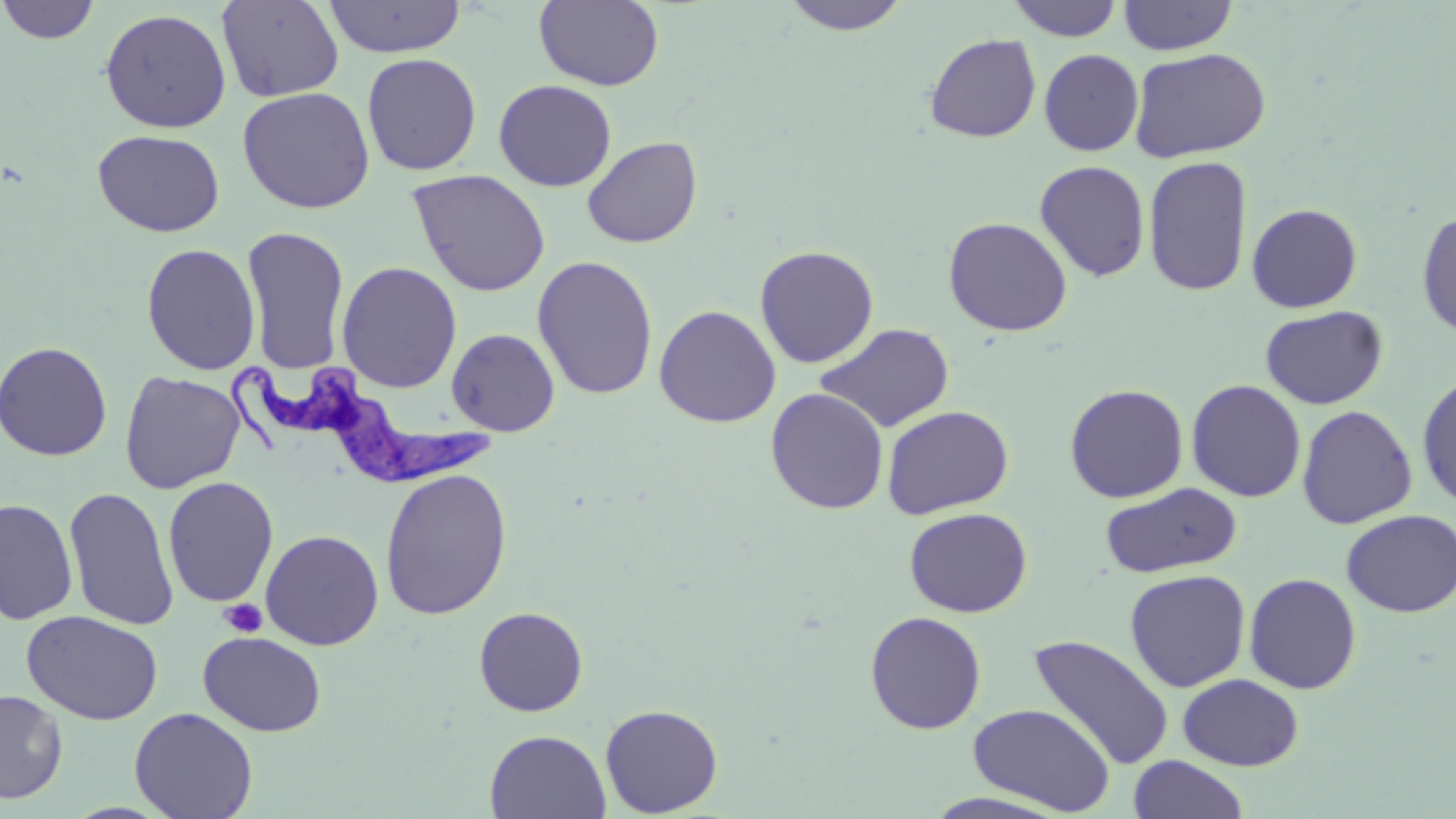
Summary:
  - Coordinate format: approximate bounding boxes as (x1,y1)-(x2,y2) corner pairs in pixels
  - Platelet locations: (219,598)-(267,638)
  - Trypanosoma brucei locations: (233,359)-(498,487)
  - Uninfected red blood cell locations: (0,0)-(101,45), (216,0)-(344,103), (534,0)-(665,91), (778,0)-(914,36), (1007,0)-(1124,41), (1118,0)-(1238,55), (323,1)-(467,58), (99,8)-(232,133), (924,33)-(1042,142), (1128,48)-(1272,163), (1039,49)-(1143,156), (362,53)-(482,176), (493,79)-(616,191), (237,86)-(375,213), (92,129)-(226,237), (582,136)-(703,249), (1143,155)-(1253,297), (1034,160)-(1151,282), (408,169)-(551,297), (1247,203)-(1363,313), (1416,210)-(1456,341), (943,216)-(1072,337), (241,226)-(350,373), (141,243)-(261,375), (754,244)-(878,368), (532,255)-(659,400), (337,261)-(462,393), (654,305)-(781,427), (1260,306)-(1389,410), (815,323)-(955,433), (446,328)-(560,437), (0,340)-(113,461), (120,370)-(245,493), (1416,372)-(1456,511), (1186,379)-(1306,502), (1064,384)-(1189,503), (765,388)-(889,514), (881,405)-(1014,519), (1297,405)-(1418,529), (379,468)-(513,620), (162,476)-(279,607), (1099,482)-(1243,579), (62,487)-(179,631), (0,497)-(78,625), (903,506)-(1032,617), (1341,509)-(1456,618), (261,530)-(384,650), (1124,569)-(1251,692), (1244,572)-(1362,694), (473,606)-(589,717), (22,610)-(163,725), (864,611)-(987,735), (198,631)-(326,736), (1028,633)-(1175,772), (1177,673)-(1304,771), (0,688)-(68,804), (600,703)-(723,817), (967,703)-(1116,815), (129,706)-(259,819), (485,729)-(610,819), (1127,755)-(1251,819), (920,791)-(1074,818)
  - Slide-level diagnosis: Trypanosoma brucei
  - Image size: 1456×819 pixels
  - Modality: optical microscopy
  - Magnification: 1000x
  - Field of view: one of a larger specimen
  - Stain: May-Grünwald-Giemsa
  - Preparation: thin blood smear